Assess this cell for malaria.
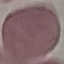
It is uninfected.

Thin smear of blood. Automatically extracted cell patch, resized to 64 × 64 pixels. Giemsa-stained preparation. Acquired by smartphone through the microscope eyepiece.